Identify the parasite.
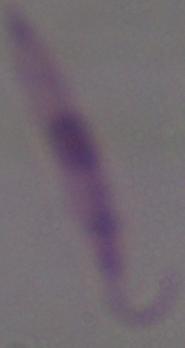

Leishmania.

Micrograph. 1000x magnification.